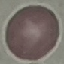
Summary:
  - Result: no malaria parasites detected
  - Stain: Giemsa
  - Image type: cell patch, automatically extracted from a larger field of view and resized to 64 × 64 pixels
  - Capture: smartphone through the microscope eyepiece
  - Preparation: thin blood film